Comment on the morphology of the red blood cells.
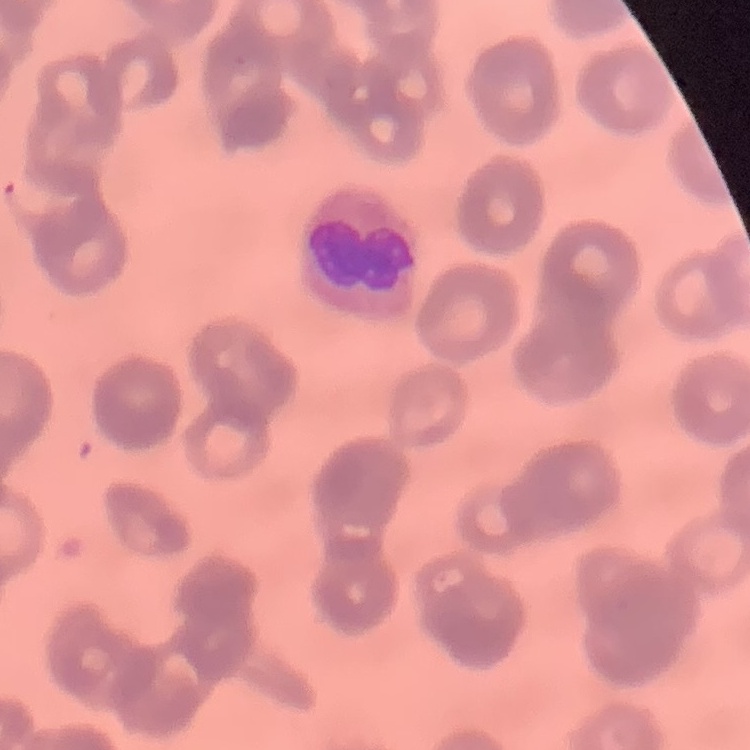
They show rouleaux formation.

Summary:
  - Stain: Field's or Giemsa
  - Image type: one tile cut from a larger photomicrograph
  - Preparation: thin blood film